Point out every Plasmodium parasite and every leukocyte.
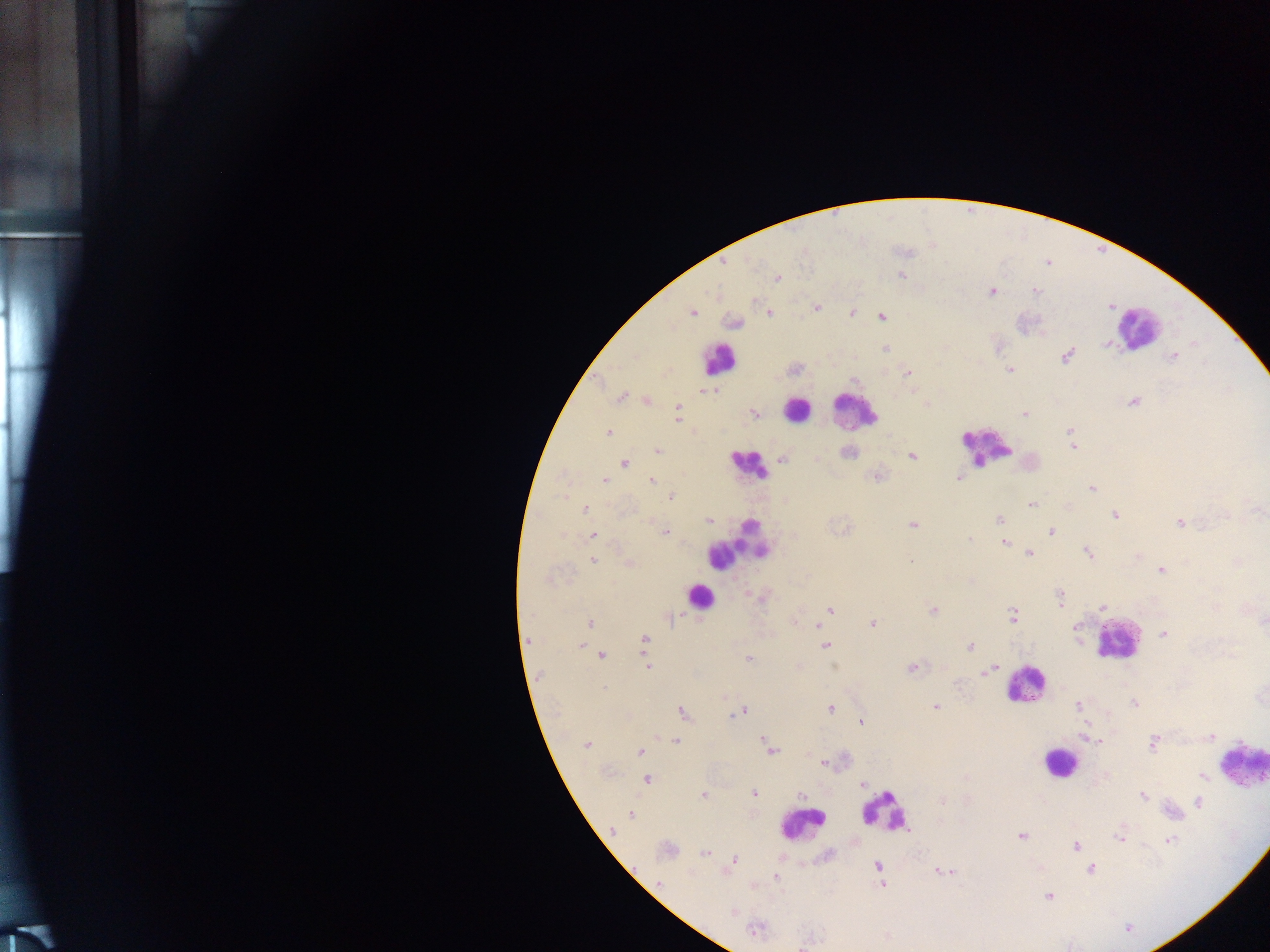

Approximate centers as (x, y) in pixels.
Plasmodium parasites: (901, 275), (779, 279), (993, 294), (817, 308), (768, 312), (852, 312), (692, 313), (855, 313), (881, 316), (732, 320), (1106, 346), (884, 348), (1068, 356), (1010, 370), (909, 373), (701, 392), (621, 397), (1134, 402), (678, 411), (752, 413), (1025, 415), (1070, 432), (609, 433), (1073, 448), (657, 450), (912, 455), (624, 464), (958, 477), (653, 479), (604, 481), (1091, 487), (562, 495), (670, 496), (1031, 504), (585, 510), (1116, 516), (1224, 517), (707, 518), (998, 518), (1180, 523), (913, 524), (1053, 532), (663, 533), (594, 534), (971, 538), (1005, 543), (1029, 553), (1087, 553), (593, 561), (911, 561), (1162, 568), (1060, 603), (1103, 608), (831, 609), (932, 610), (1013, 615), (825, 616), (592, 623), (873, 624), (817, 625), (1076, 629), (1163, 634), (1078, 636), (527, 639), (645, 640), (827, 645), (581, 646), (971, 647), (601, 654), (749, 658), (645, 661), (834, 666), (647, 668), (911, 668), (993, 670), (986, 671), (935, 706), (1077, 706), (831, 708), (745, 709), (681, 712), (738, 713), (734, 716), (861, 721), (1210, 738), (763, 740), (675, 741), (587, 743), (1153, 744), (770, 751), (641, 752), (821, 762), (1204, 776), (647, 779), (861, 784), (755, 794), (703, 795), (801, 796), (1143, 796), (1197, 802), (939, 803), (631, 814), (611, 831), (1022, 836), (1119, 837), (1170, 840), (1076, 846), (704, 853), (735, 859), (782, 859), (878, 867), (1092, 869), (774, 878), (882, 885), (1048, 896), (734, 911), (1128, 930), (803, 946).
Leukocytes: (1136, 329), (720, 358), (796, 410), (855, 410), (987, 446), (750, 463), (736, 543), (699, 597), (1118, 640), (1020, 682), (1243, 765), (1055, 767), (889, 814), (802, 826).

Summary:
  - Capture: mobile-phone photograph through a microscope
  - Field of view: single
  - Image size: 1270×952 pixels
  - Preparation: thick blood film
  - Country: Ghana